Assess this cell for malaria.
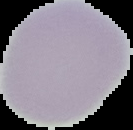

It is uninfected.

preparation = thin blood film
image type = segmented cell region with the area outside set to black
image size = 133×130 pixels